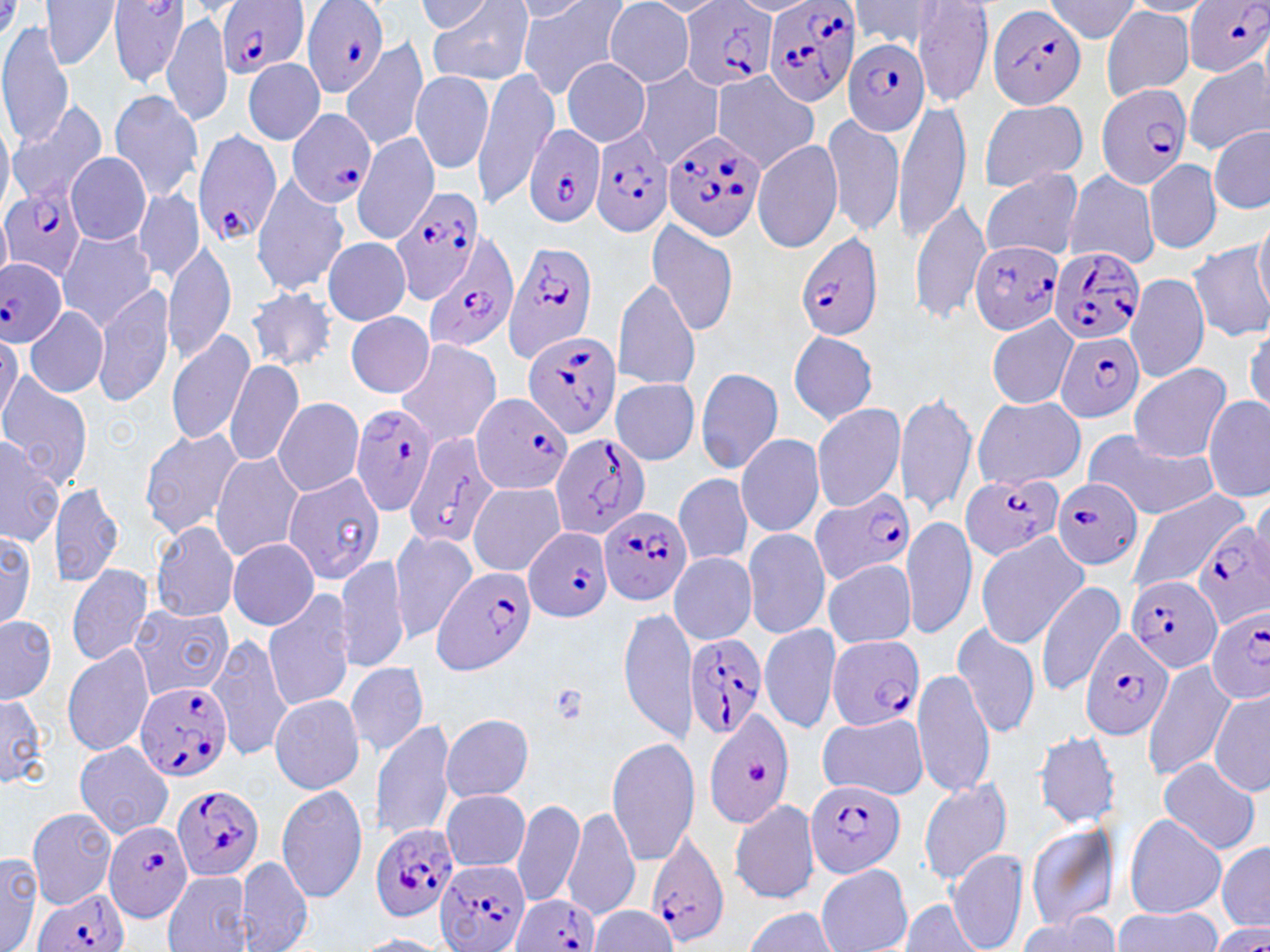

slide-level diagnosis = Plasmodium falciparum
preparation = thin blood film
modality = light microscopy
uninfected red blood cell locations (subset) = approximate bounding boxes as (x1, y1, x2, y2) in pixels: (40, 0, 120, 69), (110, 0, 190, 88), (430, 0, 535, 85), (516, 0, 632, 98), (845, 0, 948, 52), (415, 1, 494, 34), (641, 1, 730, 16), (912, 1, 993, 107), (1044, 1, 1142, 42), (1119, 1, 1215, 16), (507, 2, 593, 22), (604, 2, 695, 86), (1101, 7, 1196, 100), (162, 9, 233, 130), (0, 21, 73, 147), (340, 37, 431, 152), (244, 59, 325, 144), (562, 59, 651, 147), (1183, 60, 1269, 154), (634, 65, 724, 167), (471, 66, 562, 208), (410, 70, 496, 175), (712, 71, 821, 172), (109, 89, 205, 202), (977, 98, 1086, 193), (894, 99, 969, 242), (5, 101, 108, 205), (822, 112, 908, 239), (0, 122, 13, 213), (1209, 124, 1270, 216), (352, 131, 440, 243), (751, 138, 843, 253), (66, 152, 151, 244), (1144, 158, 1221, 255), (979, 169, 1083, 260), (1062, 169, 1160, 269), (250, 175, 349, 295), (134, 189, 202, 283), (908, 198, 991, 326), (1254, 212, 1270, 314), (646, 219, 740, 336), (57, 229, 160, 330), (322, 237, 411, 324), (164, 240, 237, 365), (1187, 243, 1270, 343), (1126, 270, 1209, 382), (612, 277, 703, 391), (94, 282, 177, 408), (243, 284, 339, 374), (24, 306, 109, 398), (346, 311, 436, 398), (987, 315, 1077, 409), (1245, 323, 1270, 417), (0, 328, 19, 429), (786, 328, 879, 425), (165, 329, 256, 448), (395, 338, 503, 447), (224, 359, 305, 469), (1129, 363, 1232, 463), (694, 367, 784, 474), (0, 373, 94, 487), (612, 378, 700, 465), (894, 390, 977, 520), (971, 396, 1085, 490), (1203, 396, 1269, 501), (272, 397, 365, 497), (810, 402, 907, 513), (138, 425, 245, 540), (1081, 427, 1218, 521), (735, 432, 825, 538), (0, 433, 62, 549), (229, 452, 360, 578), (212, 453, 305, 562), (674, 471, 753, 568), (47, 478, 124, 588), (468, 482, 566, 577), (1127, 490, 1249, 593), (1249, 490, 1270, 579), (902, 518, 976, 640), (150, 521, 240, 622), (741, 527, 831, 639), (1, 528, 37, 631), (387, 531, 477, 643), (974, 534, 1087, 648), (228, 537, 318, 630), (336, 551, 410, 671), (669, 552, 757, 643), (823, 560, 917, 647), (65, 563, 153, 666), (1035, 579, 1126, 699), (262, 589, 356, 712), (129, 604, 233, 701), (619, 608, 696, 746), (0, 614, 57, 704), (951, 621, 1041, 739), (760, 622, 843, 735), (208, 633, 292, 762), (63, 643, 155, 759), (346, 660, 430, 756), (1143, 660, 1236, 781), (912, 668, 994, 798), (1209, 690, 1270, 797), (0, 691, 50, 789), (270, 693, 364, 793), (703, 711, 796, 829), (817, 711, 929, 800), (411, 712, 531, 860), (440, 713, 535, 802), (372, 716, 458, 845), (1035, 731, 1121, 829), (606, 739, 701, 866), (73, 742, 173, 838), (1155, 757, 1262, 855), (917, 776, 1014, 884), (276, 783, 369, 905), (441, 789, 532, 872), (513, 798, 584, 908), (728, 798, 820, 905), (26, 806, 119, 906), (562, 806, 640, 923), (1122, 813, 1227, 919), (1025, 821, 1121, 931), (1216, 840, 1270, 930), (948, 848, 1029, 951), (0, 852, 44, 952), (238, 855, 313, 951), (816, 864, 912, 952), (163, 870, 252, 951), (892, 900, 988, 952), (588, 905, 675, 951), (1112, 906, 1223, 951), (741, 907, 839, 951), (1016, 913, 1119, 952), (354, 934, 453, 952)
magnification = 1000x
image size = 1270×952 pixels
platelet locations = approximate bounding boxes as (x1, y1, x2, y2) in pixels: (547, 682, 589, 727), (743, 758, 772, 784)
field of view = single
stain = May-Grünwald-Giemsa
Plasmodium falciparum-infected red blood cell locations (subset) = approximate bounding boxes as (x1, y1, x2, y2) in pixels: (761, 0, 863, 109), (1183, 0, 1270, 78), (219, 1, 310, 81), (300, 2, 388, 98), (679, 2, 778, 94), (987, 3, 1088, 109), (841, 36, 930, 137), (1096, 82, 1193, 189), (287, 109, 377, 210), (590, 123, 673, 239), (524, 125, 606, 226), (663, 128, 766, 240), (192, 129, 281, 246), (0, 184, 88, 280), (390, 186, 484, 303), (796, 232, 884, 342), (422, 234, 518, 349), (504, 238, 598, 362), (970, 240, 1064, 334), (1047, 244, 1146, 346), (0, 257, 68, 346), (524, 332, 623, 439), (1054, 332, 1145, 423), (471, 393, 572, 495), (350, 401, 438, 519), (405, 433, 503, 553), (546, 433, 652, 542), (960, 472, 1059, 562), (1051, 478, 1144, 571), (809, 486, 917, 586), (598, 504, 692, 606), (1191, 524, 1270, 627), (524, 527, 614, 622), (431, 567, 537, 675), (1127, 574, 1222, 674), (1205, 611, 1270, 703), (1079, 628, 1174, 742), (685, 632, 769, 742), (824, 634, 925, 731), (133, 682, 232, 782), (803, 781, 902, 879), (171, 784, 266, 883), (101, 819, 192, 922), (369, 823, 459, 925), (646, 831, 729, 948), (437, 860, 531, 952), (32, 889, 131, 952), (510, 895, 600, 952)